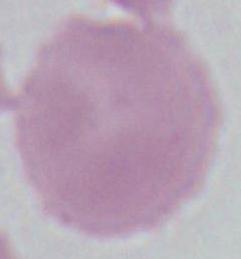

Photomicrograph. An erythrocyte is seen. 1000x magnification.